Comment on the morphology of the erythrocytes.
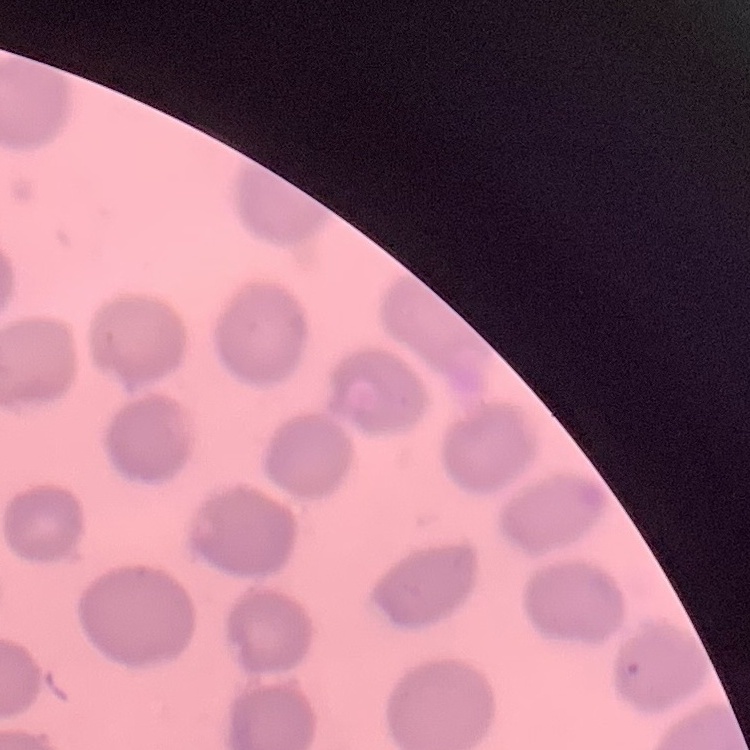

No rouleaux formation.

preparation: thin peripheral smear
image_type: one tile cut from a larger photomicrograph
stain: Field's or Giemsa